Identify the preparation type.
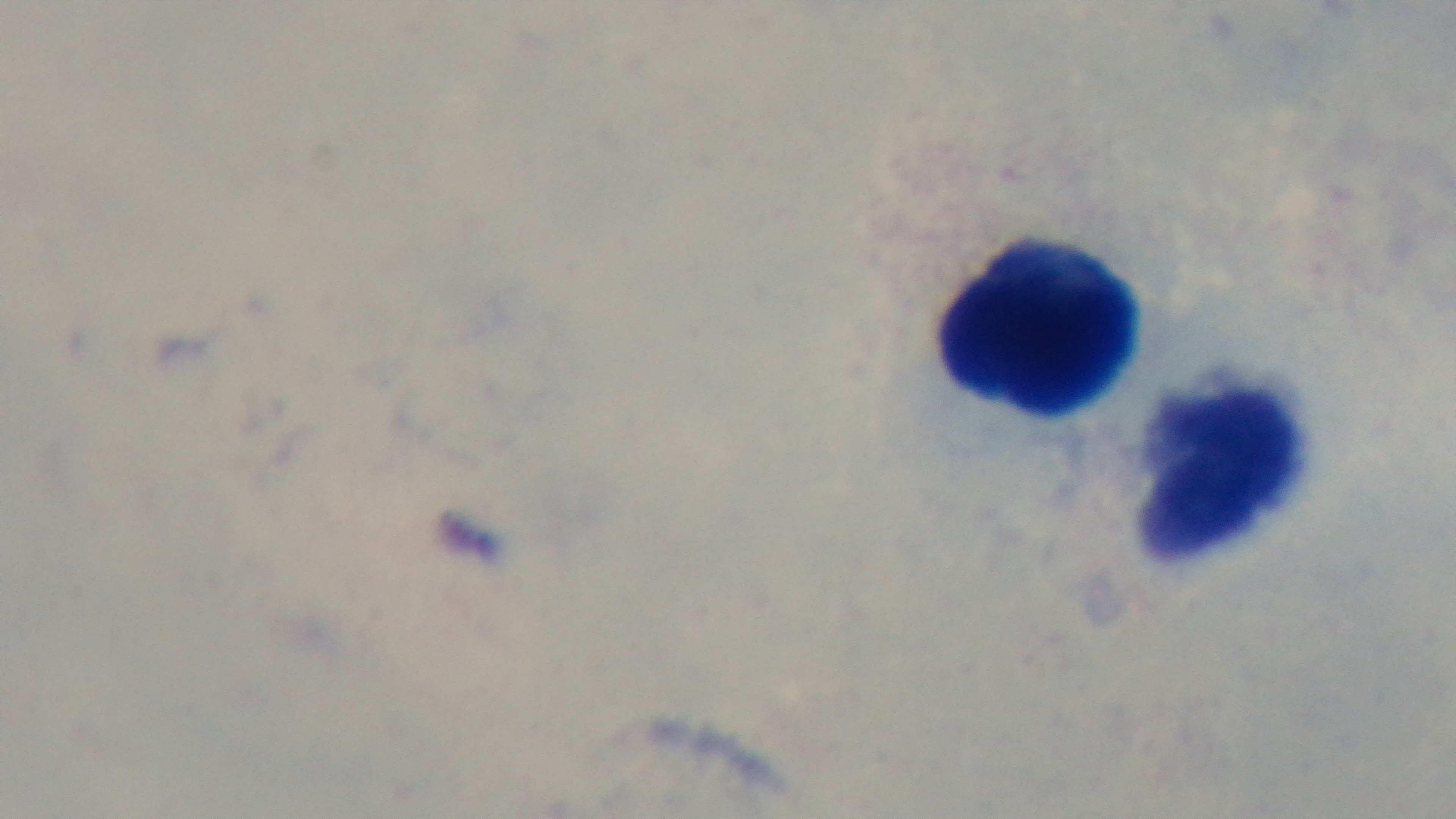
Thick.

Captured with a mounted 4K digital camera. Oil-immersion objective, 100x. Single field of view. Malaria status: negative. Giemsa-stained. Photomicrograph.